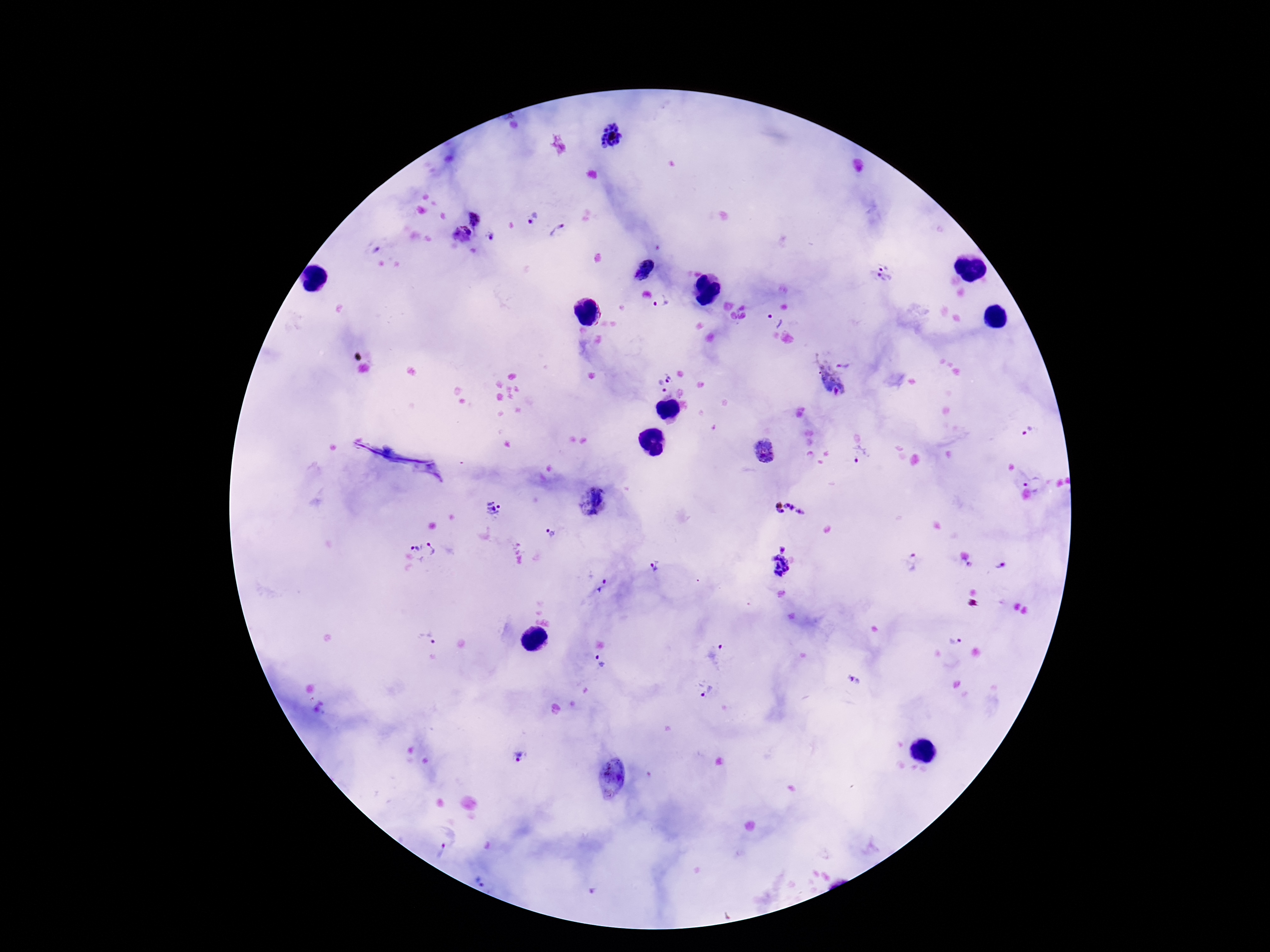

Approximate object centers, in pixels from the top-left corner.
Summary:
  - Plasmodium parasite locations: (x=614, y=137), (x=475, y=218), (x=534, y=218), (x=558, y=231), (x=461, y=236), (x=491, y=237), (x=643, y=272), (x=882, y=272), (x=661, y=303), (x=775, y=320), (x=847, y=362), (x=671, y=377), (x=829, y=382), (x=660, y=387), (x=1028, y=431), (x=764, y=454), (x=861, y=454), (x=1034, y=483), (x=594, y=501), (x=495, y=508), (x=787, y=509), (x=552, y=533), (x=783, y=548), (x=421, y=552), (x=912, y=561), (x=655, y=566), (x=779, y=566), (x=999, y=567), (x=603, y=587), (x=427, y=639), (x=955, y=641), (x=718, y=656), (x=601, y=661), (x=854, y=681), (x=706, y=692), (x=518, y=756), (x=611, y=777), (x=439, y=850), (x=486, y=886), (x=590, y=891)
  - Stain: Giemsa
  - Magnification: 100x
  - Patient malaria status: infected
  - Preparation: thick peripheral-blood smear
  - Field of view: single
  - Image size: 1270×952 pixels
  - Capture: smartphone camera through the microscope eyepiece